Report the malaria status of this cell.
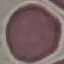

Uninfected.

image type = cell patch, automatically extracted from a larger field of view and resized to 64 × 64 pixels
capture = smartphone camera at the microscope eyepiece
stain = Giemsa
preparation = thin blood smear